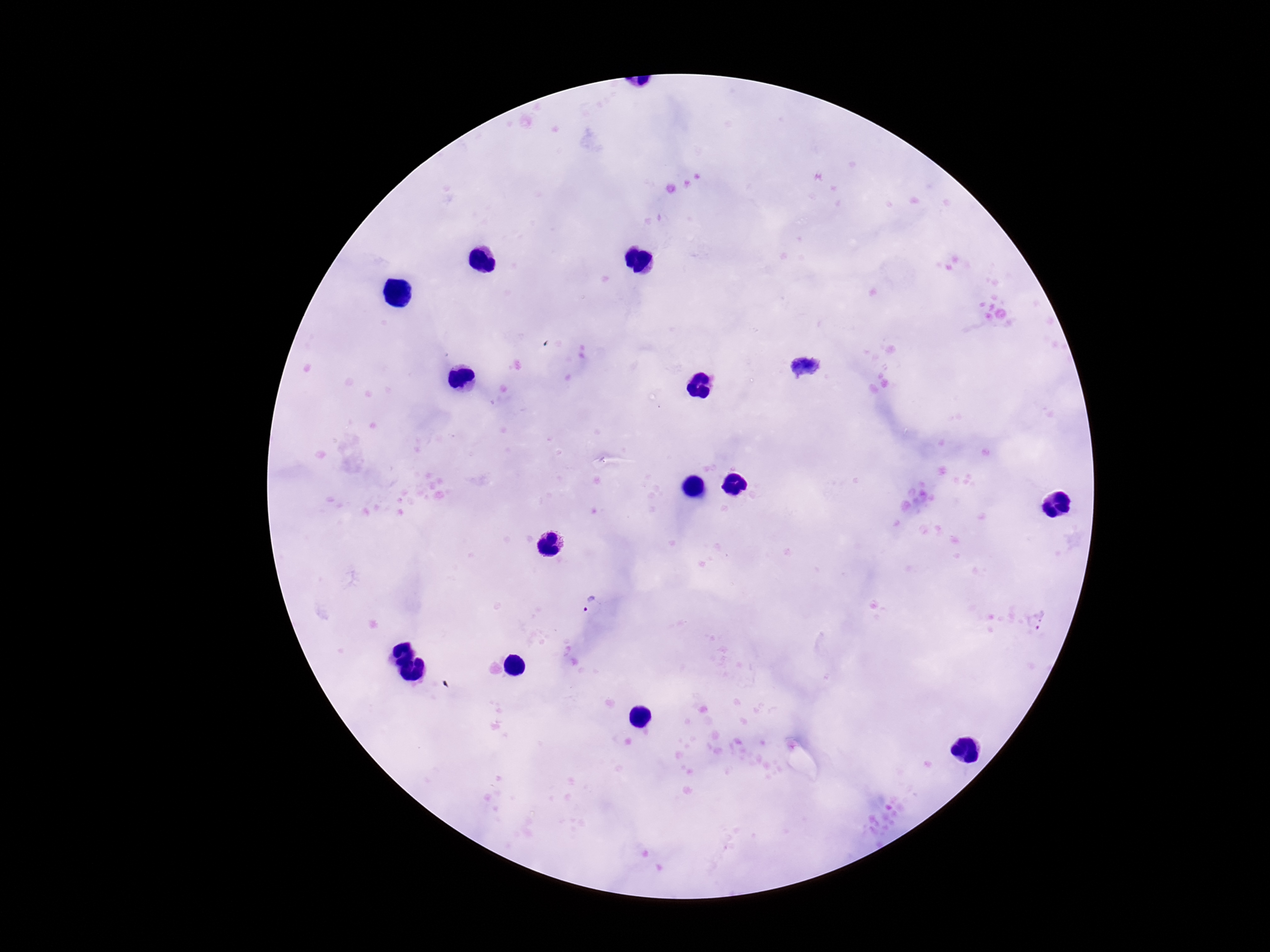

Approximate centers as [x, y] in pixels.
Summary:
  - Plasmodium parasite locations: [594, 606]
  - Image size: 1270×952 pixels
  - Stain: Giemsa
  - Patient malaria status: positive
  - Field of view: single
  - Capture: smartphone camera through the microscope eyepiece
  - Preparation: thick blood film
  - Magnification: 100x